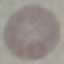

Summary:
  - Malaria status: uninfected
  - Stain: Giemsa
  - Preparation: thin blood smear
  - Image type: automatically extracted cell patch, resized to 64 × 64 pixels
  - Capture: smartphone through the microscope eyepiece